Comment on the morphology of the red blood cells.
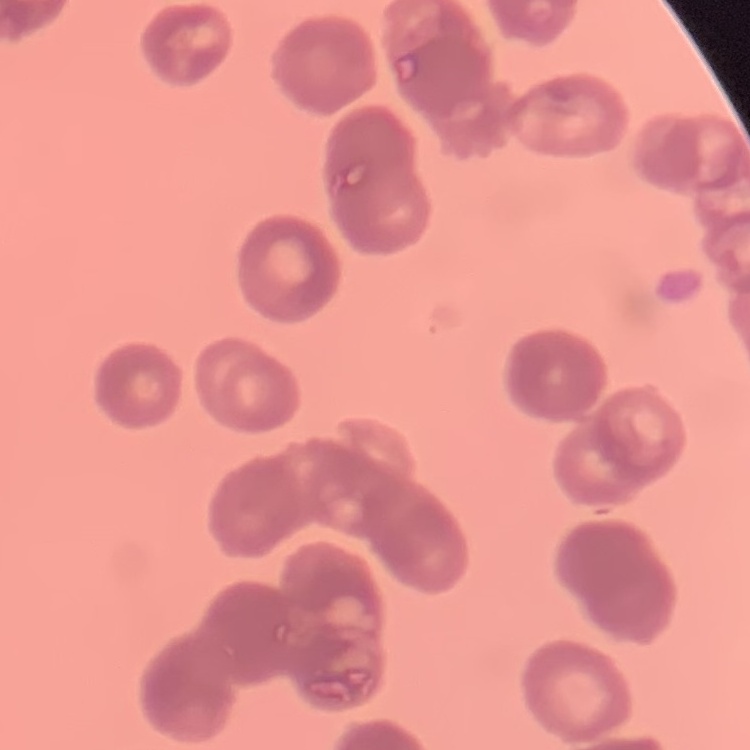
They show rouleaux formation.

stain = Field's or Giemsa
image type = one tile cut from a larger photomicrograph
preparation = thin blood smear